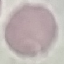

Summary:
  - Malaria status: uninfected
  - Preparation: thin blood smear
  - Image type: cell patch, automatically extracted from a larger field of view and resized to 64 × 64 pixels
  - Stain: Giemsa
  - Capture: smartphone through the microscope eyepiece